Evaluate for Plasmodium parasites.
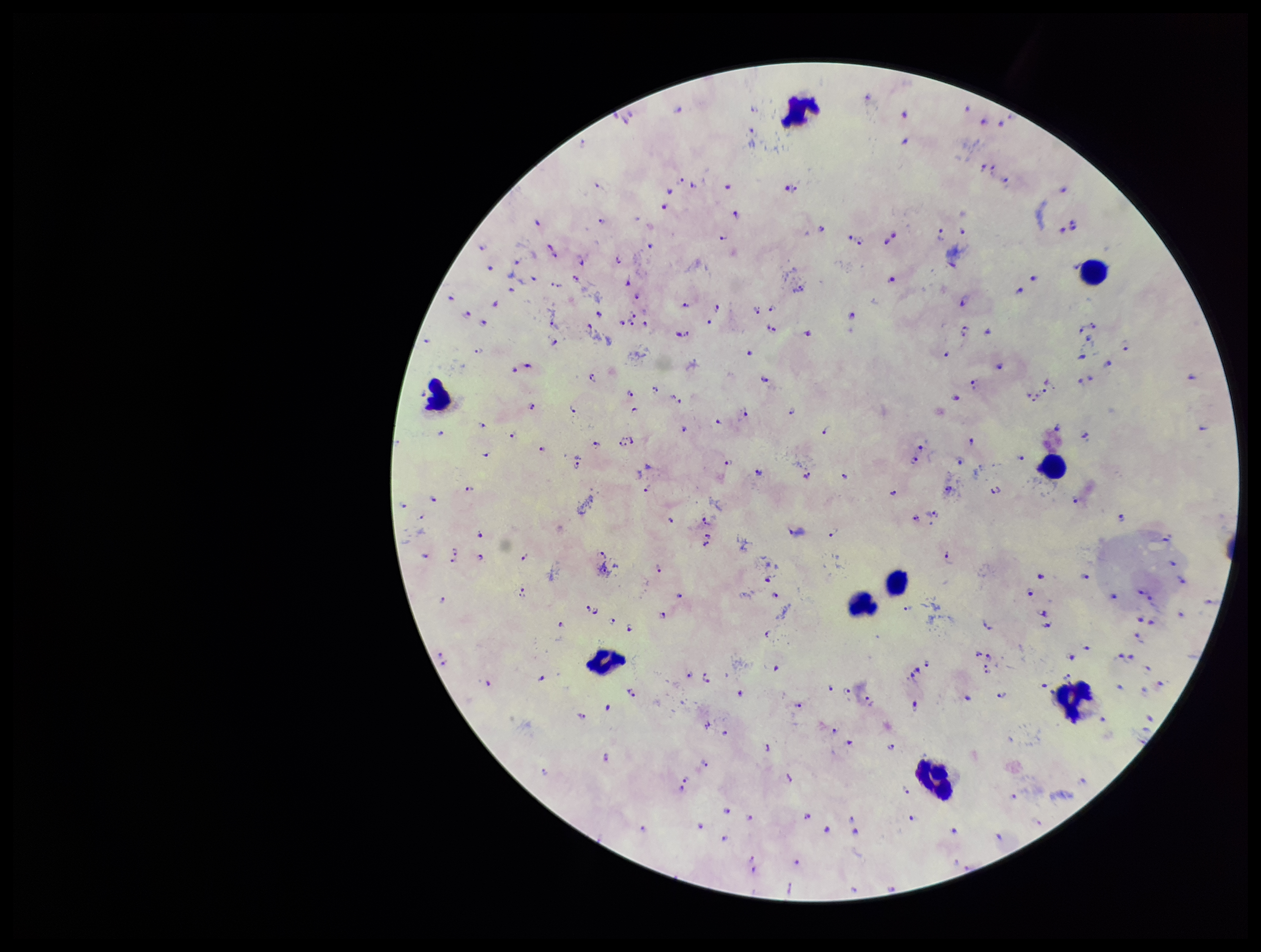

Identified.

field_of_view: one from this slide
parasite_count: 177
capture: smartphone photograph through the microscope eyepiece
patient_malaria_status: positive
image_size: 1261×952 pixels
species_reported_for_this_patient: Plasmodium falciparum
stain: Giemsa
leukocyte_count: 9
preparation: thick blood smear